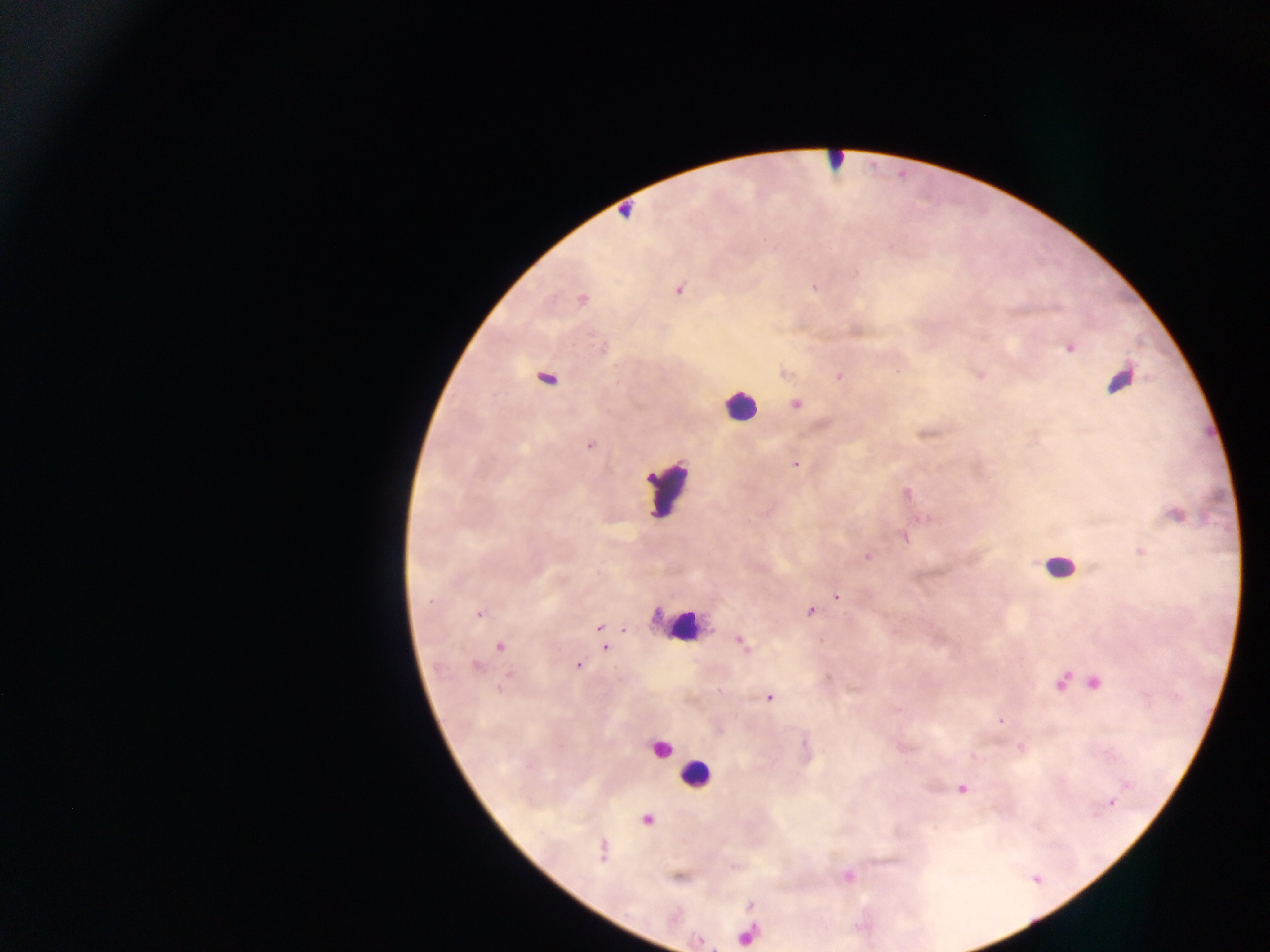 Approximate centers as (x, y) in pixels. Plasmodium parasite locations: (622, 215), (814, 284), (679, 289), (581, 299), (1069, 349), (782, 373), (796, 403), (591, 444), (796, 465), (908, 492), (835, 597), (810, 610), (480, 614), (598, 627), (743, 643), (605, 647), (577, 664), (828, 677), (770, 697), (1001, 720), (1111, 804). Leukocyte locations: (738, 404), (670, 495), (1063, 560), (684, 628), (697, 776). Image is 1270×952 pixels. Mobile-phone photograph taken through the microscope. Thick blood film. Single field of view. Sample from Ghana.